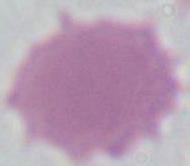

Summary:
  - Magnification: 1000x
  - Identification: erythrocyte
  - Modality: photomicrograph